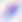

Summary:
  - Modality: photomicrograph
  - Magnification: 400x
  - Identification: Toxoplasma gondii